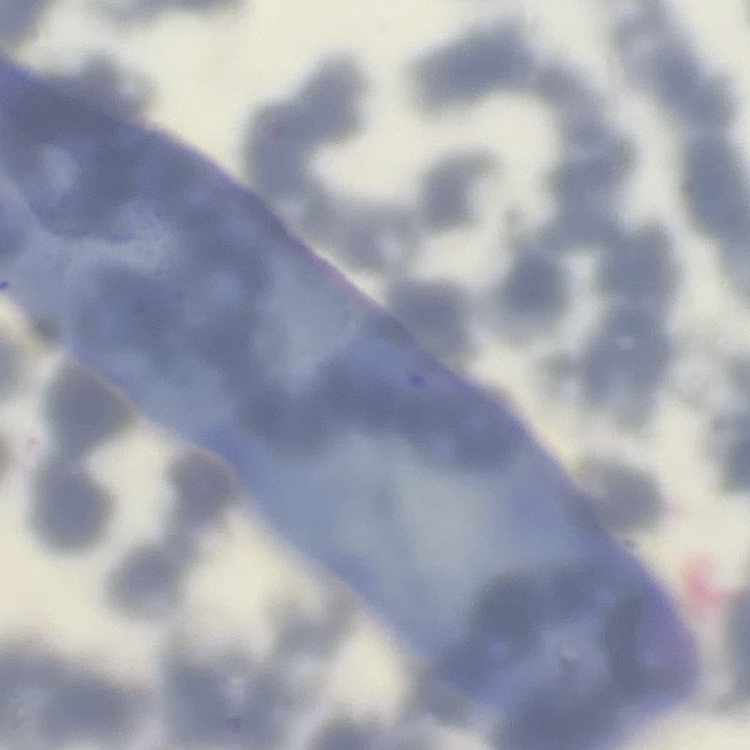

Summary:
  - Red blood cell morphology: rouleaux formation
  - Image type: square crop of a larger photomicrograph
  - Preparation: thin peripheral smear
  - Stain: Field's or Giemsa